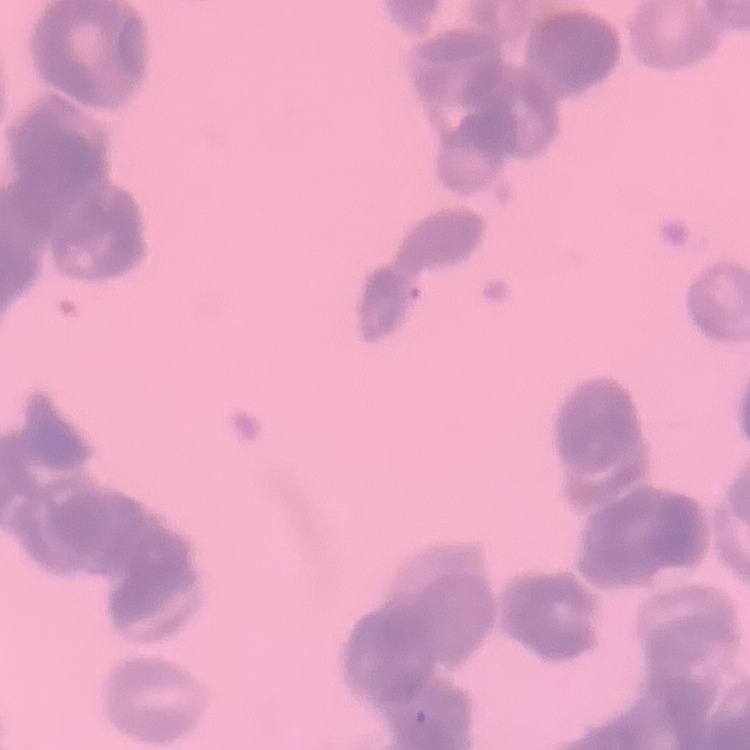

The erythrocytes show rouleaux formation. Square crop of a larger photomicrograph. Field's or Giemsa stain. Thin blood smear.